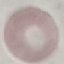
Summary:
  - Result: no malaria parasites seen
  - Capture: smartphone through the microscope eyepiece
  - Image type: cell patch, automatically extracted from a larger field of view and resized to 64 × 64 pixels
  - Preparation: thin smear
  - Stain: Giemsa